Assess this cell for malaria.
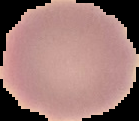
Uninfected.

Segmented cell region on a black background. Image is 139×121 pixels. From a thin blood film.